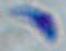

Summary:
  - Identification: Toxoplasma gondii
  - Modality: photomicrograph
  - Magnification: 1000x